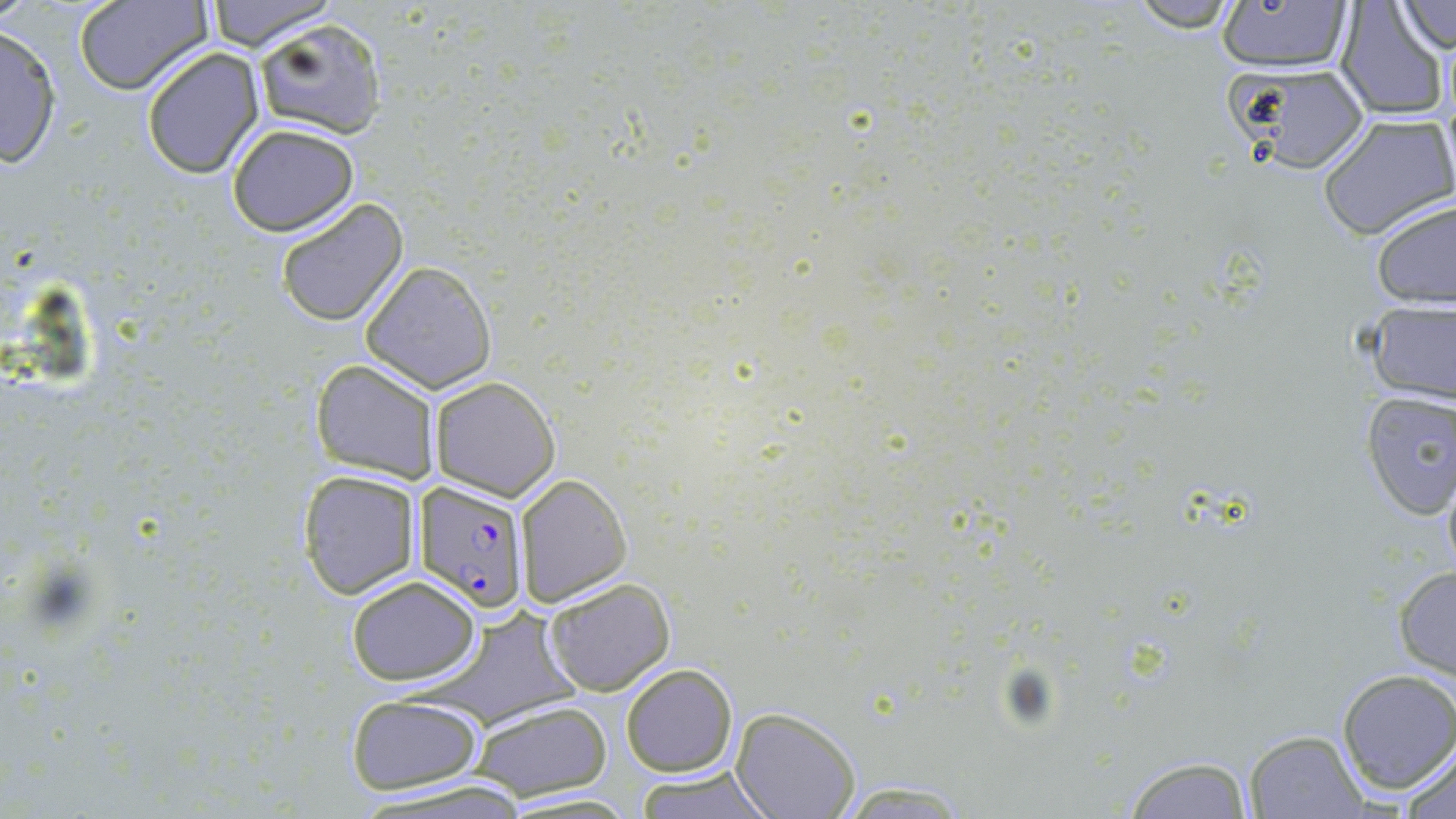
slide_level_diagnosis: Plasmodium falciparum
modality: light microscopy
plasmodium_falciparum_infected_red_blood_cell_locations: 'approximate bounding boxes as (x1,y1)-(x2,y2) corner pairs in pixels: (414,480)-(530,611)'
preparation: thin blood film
image_size: 1456×819 pixels
field_of_view: single
uninfected_red_blood_cell_locations: 'approximate bounding boxes as (x1,y1)-(x2,y2) corner pairs in pixels: (0,0)-(41,27), (73,0)-(212,96), (202,0)-(339,52), (1123,0)-(1249,33), (1212,0)-(1357,74), (1332,1)-(1451,120), (1393,3)-(1455,53), (254,20)-(388,139), (0,24)-(64,170), (141,47)-(266,179), (1224,63)-(1374,180), (1317,113)-(1454,242), (227,124)-(361,237), (274,197)-(410,328), (1369,197)-(1455,310), (359,262)-(496,393), (1359,298)-(1456,407), (310,358)-(439,484), (430,375)-(561,500), (1357,390)-(1456,519), (297,469)-(422,601), (515,474)-(634,606), (1393,568)-(1456,681), (345,574)-(483,686), (543,577)-(675,696), (621,662)-(739,777), (1335,669)-(1455,794), (346,693)-(485,795), (468,700)-(614,801), (730,707)-(861,819), (1244,730)-(1369,818), (1401,742)-(1456,819), (1118,755)-(1256,818), (632,765)-(779,819), (829,777)-(975,816)'
magnification: 1000x
stain: May-Grünwald-Giemsa